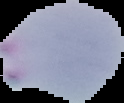

Summary:
  - Image size: 124×103 pixels
  - Malaria status: parasitized
  - Image type: segmented cell region with the area outside set to black
  - Preparation: thin blood film